Locate every white blood cell.
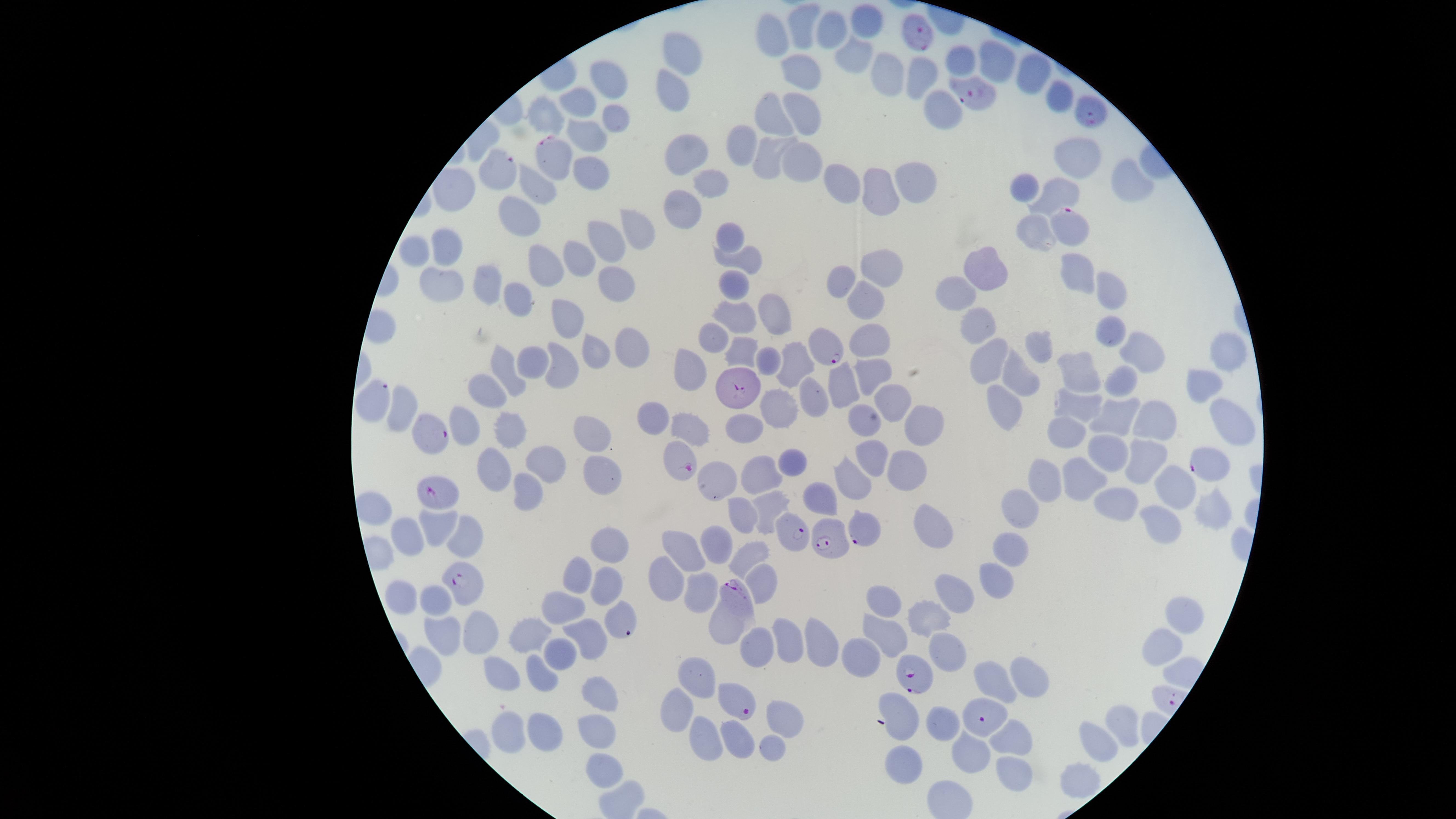
No white blood cells identified.

Approximate marker points as [x, y] in pixels. Parasitized red blood cells: [914, 31], [975, 90], [1090, 111], [555, 155], [500, 167], [1076, 232], [825, 342], [735, 391], [376, 395], [430, 432], [1202, 465], [684, 466], [436, 497], [860, 529], [796, 532], [830, 542], [458, 583], [734, 592], [913, 677], [736, 704], [985, 718]. Uninfected red blood cells: [802, 22], [867, 24], [831, 33], [773, 37], [691, 49], [854, 55], [997, 58], [961, 59], [1036, 69], [802, 70], [893, 73], [927, 75], [612, 80], [672, 94], [582, 100], [772, 103], [944, 106], [801, 109], [548, 110], [622, 117], [586, 132], [742, 143], [1075, 149], [686, 151], [768, 153], [800, 155], [595, 170], [1133, 180], [921, 183], [710, 185], [851, 185], [1022, 185], [540, 187], [884, 187], [1061, 192], [684, 200], [523, 214], [636, 223], [1035, 234], [602, 237], [730, 237], [449, 242], [420, 248], [749, 252], [577, 256], [991, 263], [546, 264], [885, 264], [1080, 272], [841, 278], [487, 280], [733, 280], [445, 283], [1117, 284], [619, 285], [956, 292], [518, 296], [869, 307], [735, 312], [774, 314], [566, 316], [977, 322], [713, 330], [1111, 331], [868, 339], [1043, 342], [632, 346], [1139, 348], [746, 352], [588, 354], [1217, 354], [768, 359], [991, 360], [799, 362], [538, 363], [509, 366], [685, 367], [1081, 369], [562, 370], [868, 375], [1018, 377], [1122, 379], [837, 383], [1202, 387], [494, 388], [814, 393], [901, 396], [1002, 396], [1082, 399], [780, 404], [403, 407], [1117, 411], [652, 415], [859, 418], [466, 419], [1233, 419], [748, 420], [1155, 420], [918, 421], [691, 423], [510, 427], [596, 435], [1069, 439], [1112, 449], [1146, 449], [874, 457], [790, 461], [551, 463], [502, 467], [909, 469], [761, 475], [1053, 477], [596, 480], [719, 481], [851, 481], [1087, 482], [1169, 490], [525, 492], [824, 495], [1026, 501], [1120, 503], [770, 505], [373, 510], [744, 513], [1211, 514], [434, 522], [1164, 523], [932, 527], [464, 533], [406, 536], [1011, 537], [714, 540], [682, 546], [614, 547], [752, 552], [576, 575], [998, 576], [662, 579], [599, 580], [763, 581], [705, 590], [957, 591], [407, 598], [883, 599], [439, 602], [566, 610], [1180, 610], [924, 616], [721, 623], [476, 630], [533, 630], [885, 633], [442, 634], [592, 635], [787, 640], [821, 641], [758, 650], [1152, 650], [561, 651], [858, 653], [949, 655], [536, 672], [705, 674], [508, 675], [1021, 677], [989, 680], [602, 695], [898, 710], [674, 715], [779, 718], [940, 724], [1123, 724], [540, 730], [595, 731], [512, 734], [740, 735], [708, 739], [1094, 739], [1010, 740], [769, 747], [963, 755], [900, 758], [601, 764], [1010, 777], [1077, 782]. Presence: malaria parasites detected. The visible region is circular. Image is 1456×819 pixels. Giemsa-stained preparation. Species: Plasmodium falciparum. Thin blood smear. Single field of view. Smartphone photograph through the microscope eyepiece.